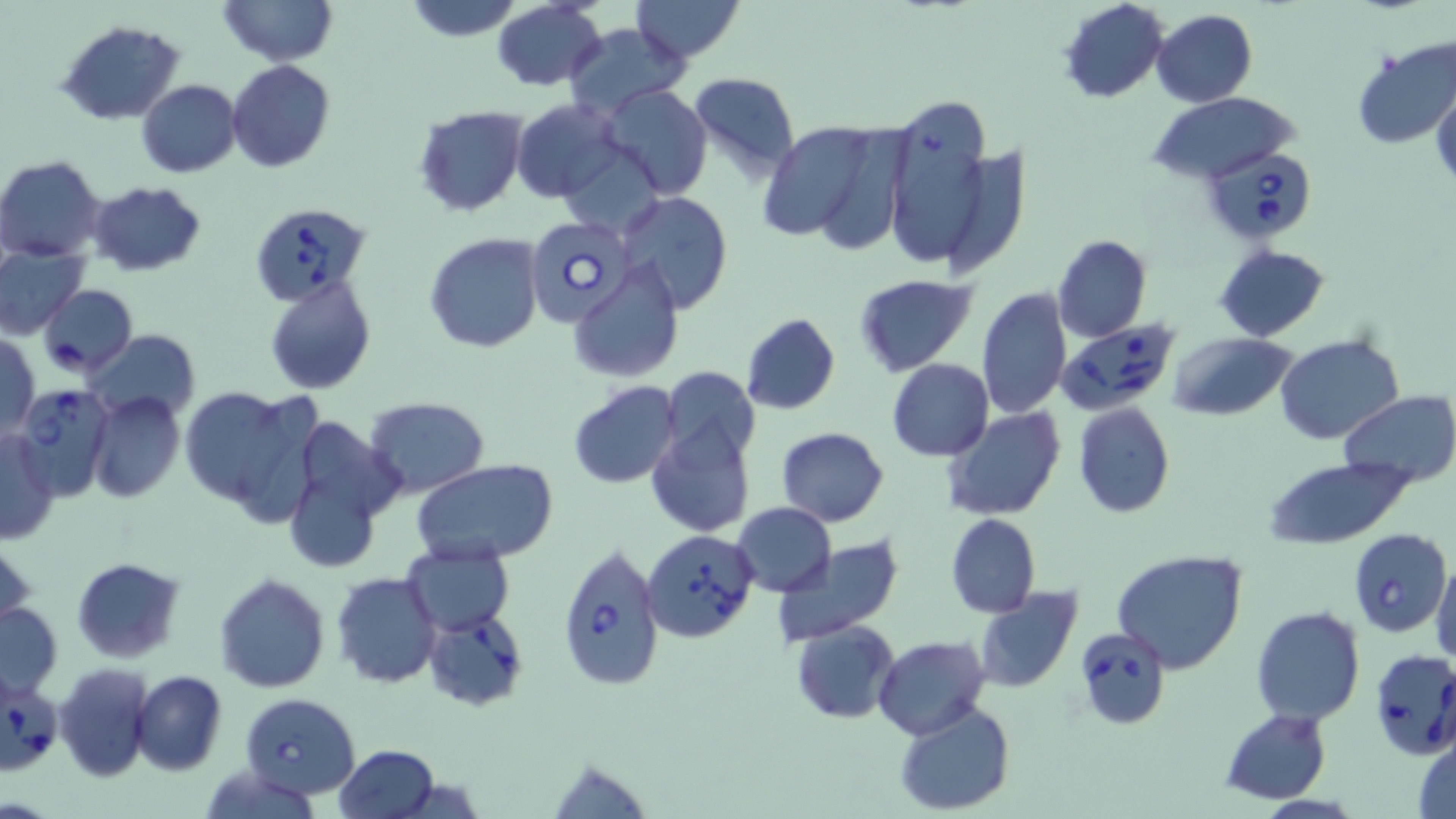
Summary:
  - Coordinate format: approximate bounding boxes as (x1, y1, x2, y2) in pixels
  - Babesia divergens-infected red blood cell locations: (1204, 143, 1318, 243), (251, 200, 371, 306), (523, 215, 635, 328), (1055, 318, 1178, 414), (12, 385, 116, 497), (642, 529, 759, 642), (1350, 529, 1451, 637), (555, 542, 664, 692), (424, 609, 527, 711), (1075, 629, 1171, 729), (1370, 649, 1456, 759), (1, 674, 62, 776), (239, 692, 361, 799)
  - Uninfected red blood cell locations: (217, 0, 337, 65), (403, 0, 525, 41), (631, 0, 744, 62), (490, 1, 608, 91), (1059, 1, 1170, 104), (1153, 10, 1256, 108), (57, 20, 185, 125), (565, 22, 686, 115), (1352, 36, 1456, 149), (227, 59, 334, 172), (686, 71, 801, 180), (136, 79, 241, 178), (1431, 82, 1456, 187), (601, 84, 713, 200), (1147, 92, 1298, 185), (510, 99, 625, 202), (877, 99, 996, 271), (412, 107, 527, 217), (757, 116, 902, 248), (559, 144, 665, 239), (936, 144, 1032, 281), (0, 155, 107, 262), (85, 180, 208, 278), (614, 192, 736, 315), (423, 233, 545, 352), (1052, 235, 1151, 342), (1214, 244, 1329, 343), (0, 246, 88, 339), (570, 262, 684, 383), (853, 274, 978, 376), (265, 279, 377, 394), (36, 284, 137, 377), (977, 287, 1073, 420), (739, 313, 841, 414), (80, 330, 202, 422), (1168, 332, 1298, 421), (2, 333, 40, 438), (1275, 333, 1404, 444), (887, 359, 994, 461), (657, 367, 761, 468), (569, 381, 682, 488), (179, 383, 321, 521), (1337, 390, 1454, 486), (85, 391, 185, 504), (364, 398, 490, 496), (1072, 402, 1175, 519), (942, 409, 1066, 522), (278, 413, 404, 576), (647, 420, 755, 537), (777, 427, 888, 526), (0, 429, 58, 546), (1262, 456, 1411, 550), (413, 460, 556, 567), (733, 502, 837, 596), (946, 513, 1041, 618), (1, 536, 35, 633), (774, 537, 904, 648), (401, 546, 514, 635), (1110, 548, 1249, 674), (72, 557, 185, 662), (1430, 557, 1456, 667), (214, 572, 331, 693), (331, 572, 442, 690), (975, 586, 1082, 693), (1, 602, 63, 696), (1248, 606, 1365, 727), (792, 620, 900, 724), (875, 636, 990, 740), (54, 663, 153, 783), (132, 670, 226, 776), (893, 701, 1016, 816), (1219, 708, 1331, 805), (1413, 732, 1456, 819), (335, 744, 439, 819), (545, 755, 656, 819), (196, 763, 325, 819)
  - Slide-level diagnosis: Babesia divergens
  - Image size: 1456×819 pixels
  - Preparation: thin blood smear
  - Stain: May-Grünwald-Giemsa
  - Modality: light microscopy
  - Magnification: 1000x
  - Field of view: single